State which cell type is depicted.
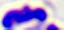

This is a leukocyte.

400x magnification. Photomicrograph.